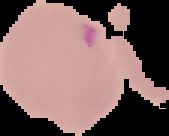 From a thin blood smear. Segmented cell region on a black background. Result: Plasmodium parasites identified. Image is 169×136 pixels.